Point out each Plasmodium parasite.
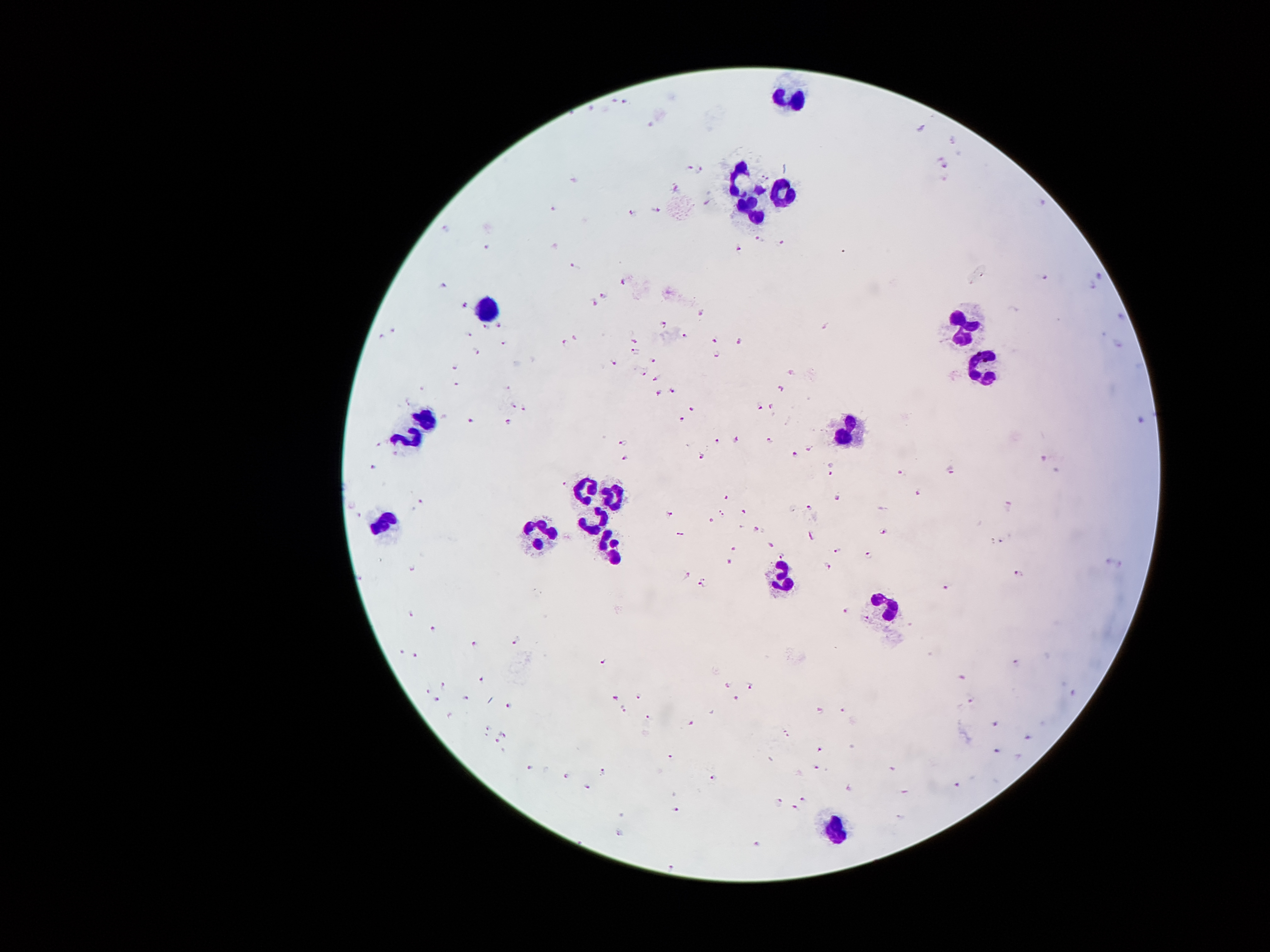

Approximate centers as [x, y] in pixels.
Plasmodium parasites: [625, 100], [921, 128], [945, 166], [699, 170], [573, 180], [676, 188], [657, 210], [556, 212], [629, 213], [445, 229], [757, 240], [779, 244], [486, 248], [739, 250], [841, 252], [573, 264], [1043, 277], [623, 283], [444, 287], [605, 296], [593, 305], [464, 306], [701, 313], [500, 326], [662, 326], [484, 328], [824, 328], [393, 330], [469, 337], [687, 337], [382, 338], [714, 340], [633, 341], [738, 342], [504, 343], [566, 345], [478, 350], [635, 352], [717, 355], [653, 359], [610, 363], [455, 367], [643, 371], [655, 378], [458, 385], [507, 388], [779, 390], [671, 391], [659, 394], [513, 406], [757, 406], [693, 407], [774, 407], [525, 408], [508, 420], [682, 420], [468, 421], [736, 440], [625, 441], [716, 441], [770, 444], [377, 445], [808, 448], [796, 454], [703, 456], [626, 459], [1041, 462], [373, 466], [831, 468], [949, 468], [901, 474], [563, 484], [918, 494], [722, 497], [839, 500], [421, 502], [1011, 507], [808, 509], [721, 512], [743, 512], [671, 515], [712, 522], [755, 529], [881, 531], [999, 541], [770, 548], [735, 550], [837, 551], [869, 554], [782, 558], [731, 563], [828, 565], [413, 567], [1019, 575], [686, 576], [702, 583], [943, 589], [844, 611], [413, 616], [435, 630], [515, 642], [475, 645], [401, 651], [416, 657], [603, 661], [1014, 662], [961, 676], [481, 680], [749, 684], [443, 685], [728, 687], [427, 689], [615, 697], [637, 699], [735, 699], [438, 700], [466, 700], [969, 700], [510, 704], [841, 709], [624, 710], [818, 710], [648, 715], [690, 724], [994, 724], [488, 730], [503, 734], [786, 734], [1028, 737], [496, 742], [995, 750], [821, 751], [671, 757], [817, 766], [530, 768], [602, 772], [566, 775], [713, 779], [956, 784], [588, 787], [802, 799], [781, 801], [795, 809], [675, 810], [617, 833].

Leukocyte locations: [791, 96], [742, 182], [782, 191], [751, 211], [484, 308], [961, 328], [985, 363], [426, 419], [846, 429], [408, 438], [589, 485], [610, 495], [382, 521], [596, 521], [541, 534], [607, 546], [777, 577], [884, 607], [835, 826]. Patient malaria status: positive for Plasmodium falciparum. 100x magnification. Single field of view. Photographed through the microscope eyepiece with a smartphone camera. Image is 1270×952 pixels. Giemsa-stained preparation. Thick blood film.